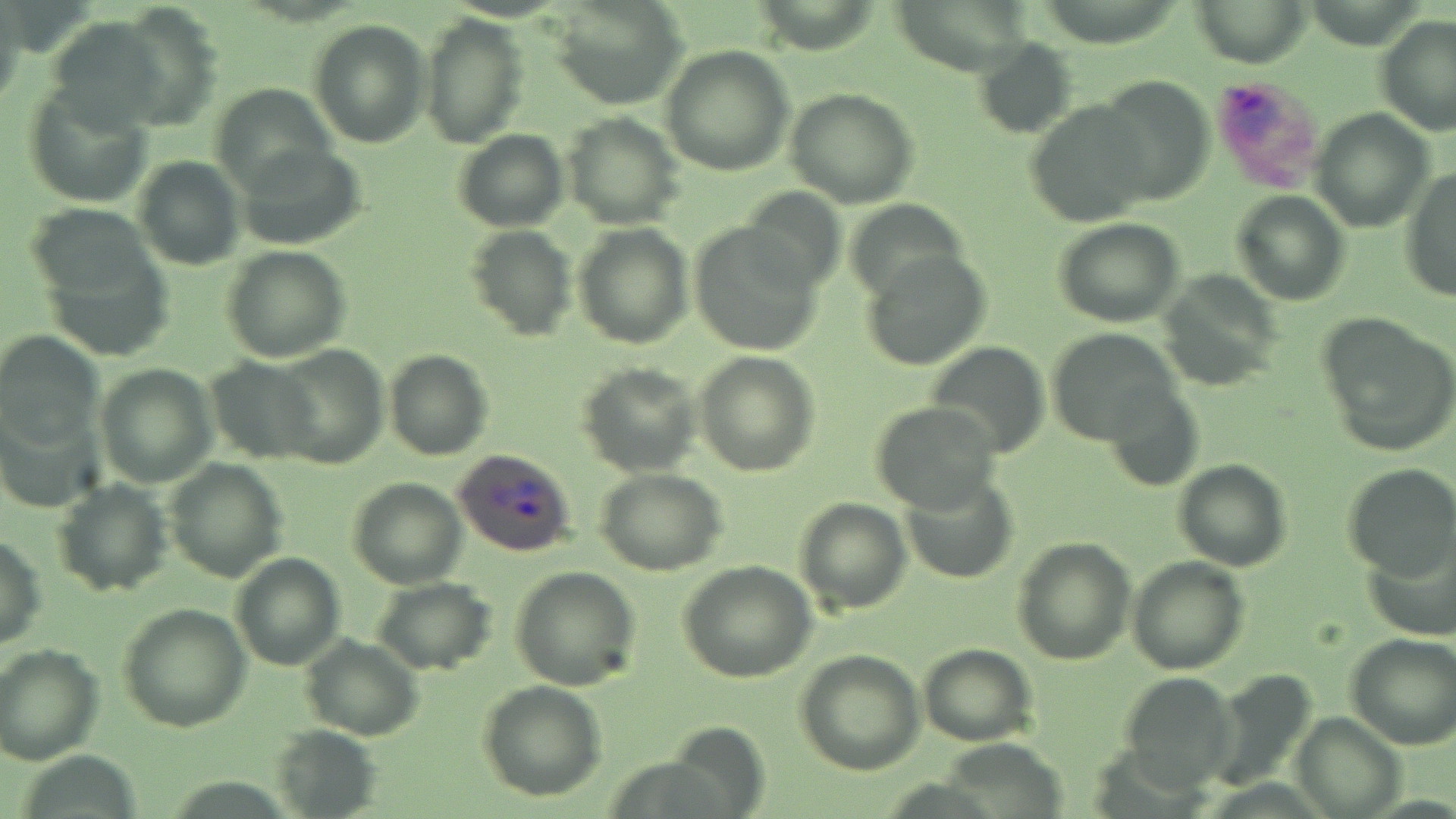

Approximate bounding boxes as (x1,y1)-(x2,y2) corner pairs in pixels. Uninfected red blood cell locations: (1188,0)-(1316,67), (112,2)-(222,129), (550,2)-(688,111), (416,13)-(529,149), (47,14)-(174,128), (1373,14)-(1456,138), (308,19)-(432,148), (974,39)-(1079,140), (660,46)-(794,176), (1092,76)-(1212,206), (23,81)-(156,207), (210,81)-(338,191), (785,88)-(919,207), (1024,98)-(1155,227), (1309,110)-(1432,231), (562,111)-(685,229), (454,129)-(568,232), (236,144)-(367,250), (132,156)-(244,271), (1401,169)-(1455,302), (740,187)-(844,298), (1231,191)-(1351,305), (843,199)-(968,305), (27,204)-(160,307), (1053,217)-(1185,327), (688,222)-(827,355), (572,223)-(692,349), (465,225)-(576,342), (221,245)-(352,363), (861,249)-(991,371), (1160,270)-(1286,391), (1317,314)-(1456,457), (1045,328)-(1183,446), (0,330)-(104,450), (926,340)-(1051,457), (269,346)-(389,469), (385,349)-(494,460), (694,350)-(821,479), (204,356)-(324,462), (94,361)-(218,486), (577,363)-(702,477), (1102,380)-(1203,490), (869,400)-(1003,512), (163,457)-(288,583), (1171,458)-(1292,571), (1341,463)-(1456,580), (595,469)-(729,575), (899,471)-(1019,584), (347,477)-(467,588), (52,478)-(172,596), (794,496)-(912,615), (0,535)-(48,650), (1012,536)-(1137,666), (1359,537)-(1455,642), (230,553)-(346,671), (1127,556)-(1250,675), (675,560)-(817,683), (510,565)-(641,691), (369,577)-(496,674), (118,602)-(251,734), (1344,634)-(1455,750), (300,636)-(424,740), (918,644)-(1037,746), (0,645)-(104,766), (795,650)-(926,775), (1213,667)-(1318,786), (1116,670)-(1239,790), (477,680)-(607,802), (1291,712)-(1405,819), (270,725)-(384,817), (940,739)-(1066,816). Plasmodium ovale-infected red blood cell locations: (1208,71)-(1327,192), (451,449)-(576,558). Slide-level diagnosis: Plasmodium ovale. Captured at 1000x magnification. Light microscopy. Image is 1456×819 pixels. May-Grünwald-Giemsa stain. Single field of view. Thin blood film.